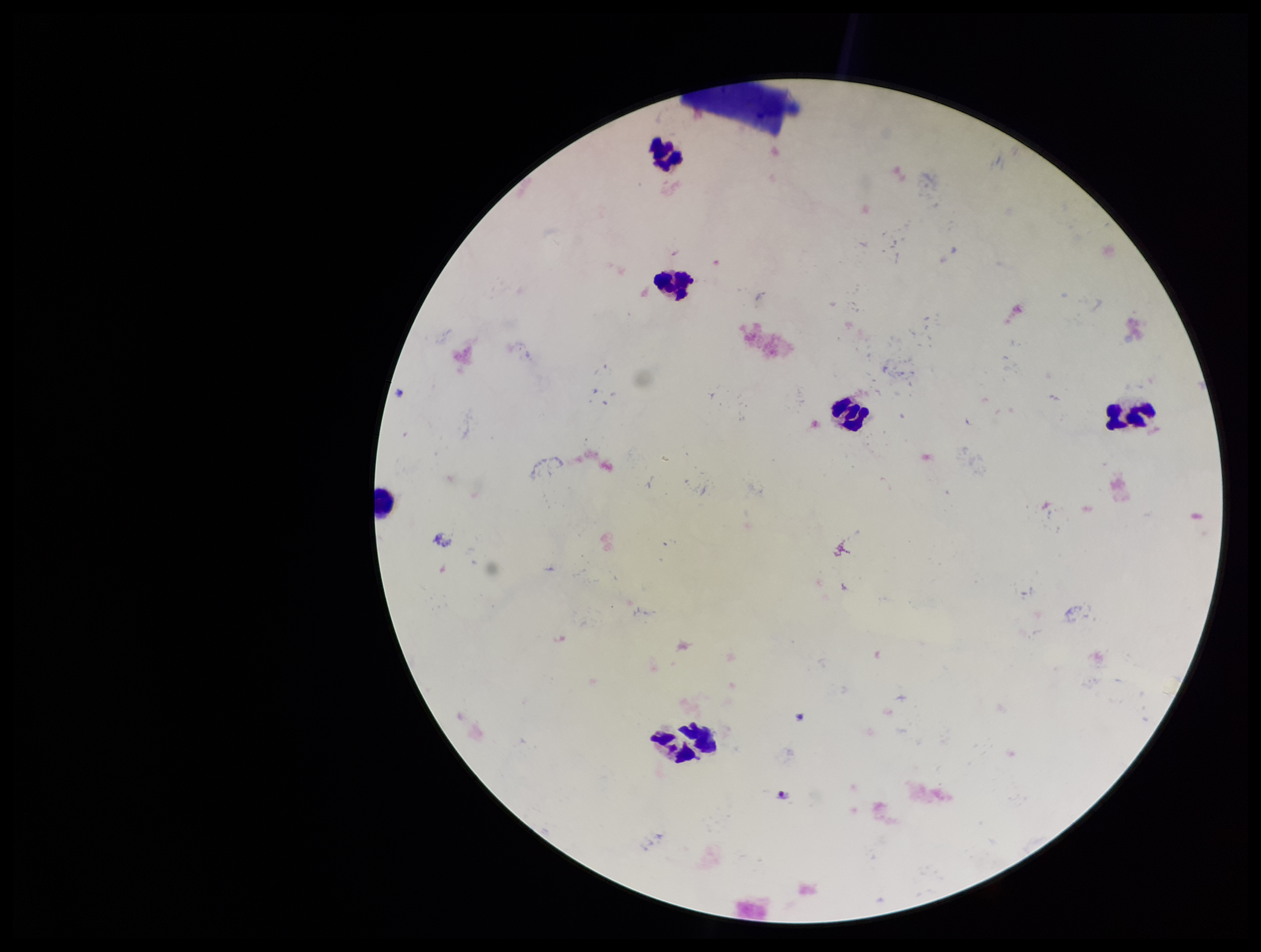

patient malaria status = negative
capture = smartphone photograph through the microscope eyepiece
Plasmodium parasites = none seen
parasite count = 0
leukocyte count = 6
image size = 1261×952 pixels
field of view = one from this slide
stain = Giemsa
preparation = thick blood smear